Classify this cell by malaria status.
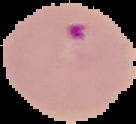
Parasitized.

Summary:
  - Image size: 136×124 pixels
  - Image type: cell region segmented out of the field of view; surrounding area masked to black
  - Preparation: thin blood film